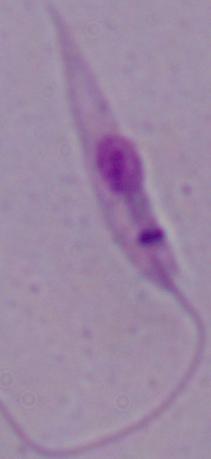

modality: micrograph
magnification: 1000x
identification: Leishmania